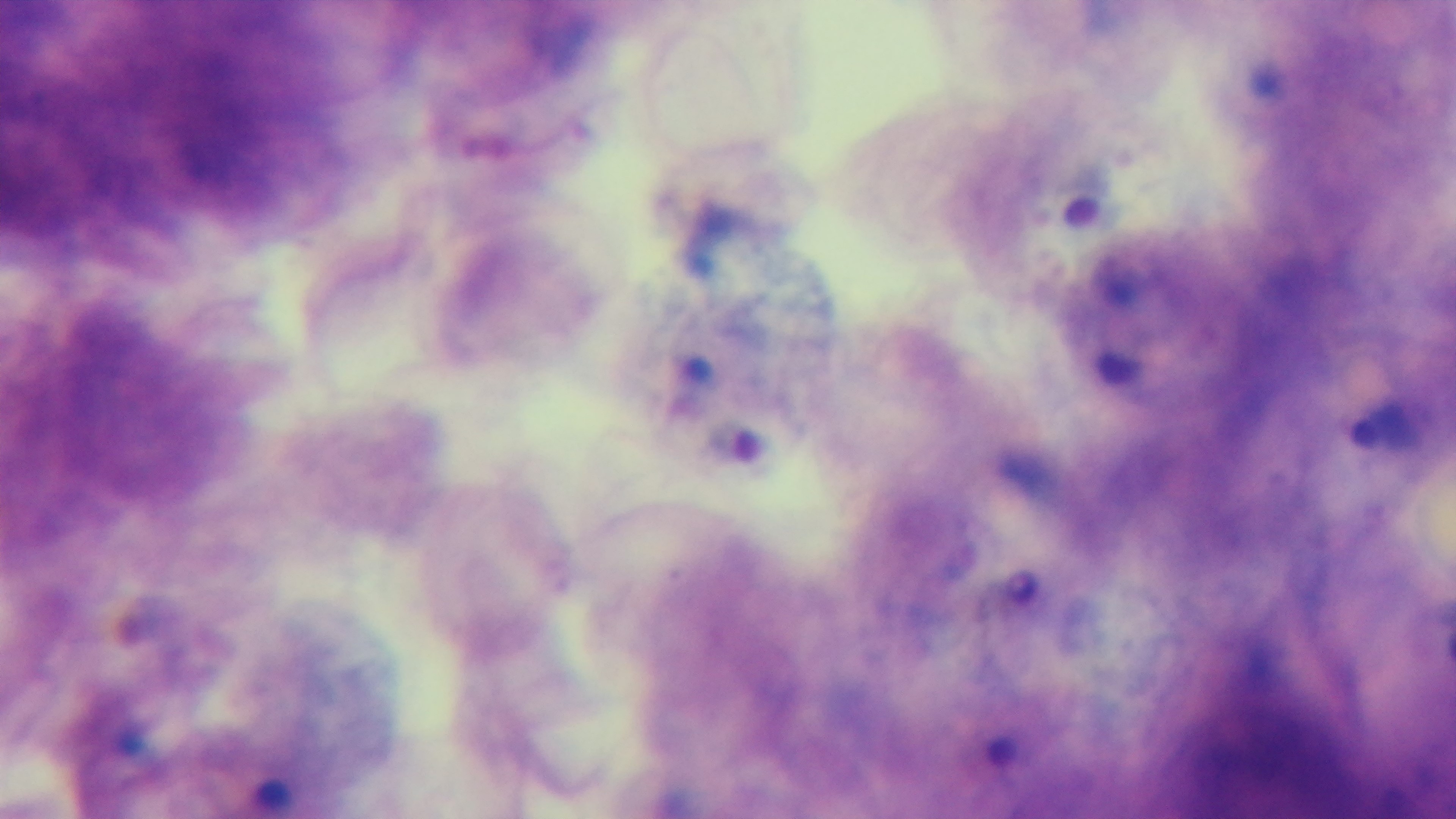

Summary:
  - Stain: Giemsa
  - Malaria status: positive
  - Modality: light microscopy
  - Objective: 100x oil immersion
  - Capture: mounted 4K digital camera
  - Field of view: one from the slide
  - Preparation: thick smear